Describe the morphology of the red blood cells.
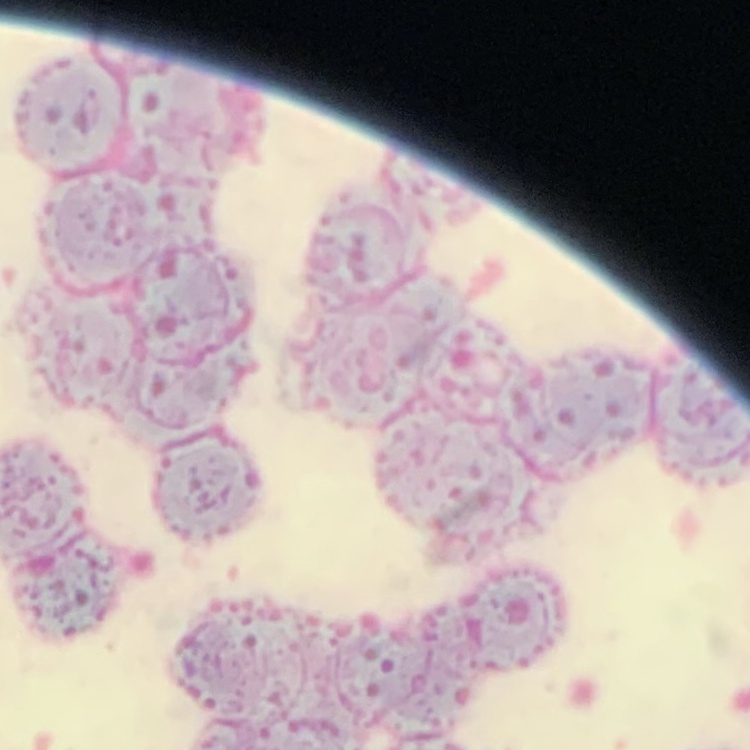
They show rouleaux formation.

Summary:
  - Preparation: thin blood film
  - Stain: Field's or Giemsa
  - Image type: square crop of a larger photomicrograph